Give the position of every malaria parasite.
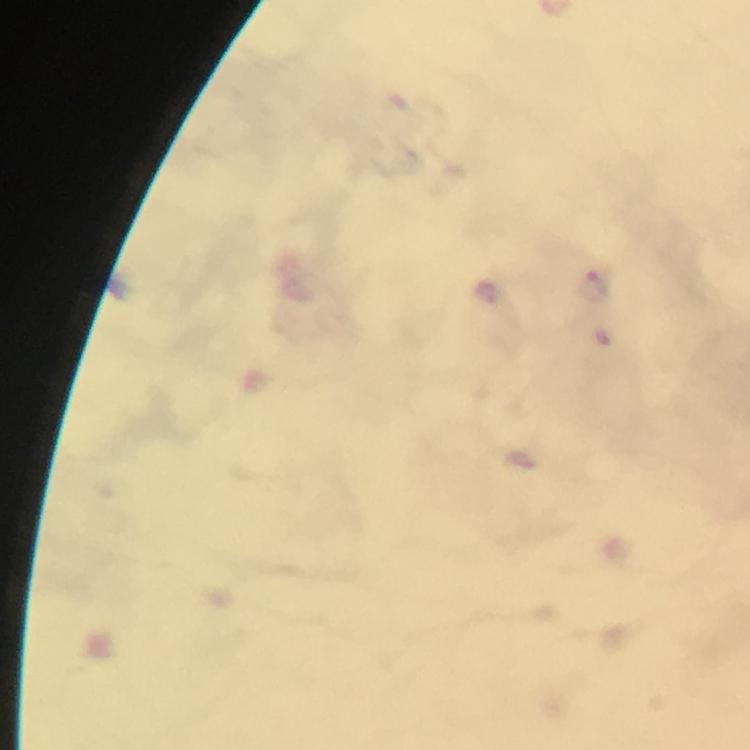

Approximate centers as {x, y} in pixels.
Malaria parasites: {593, 283}, {487, 294}.

100x magnification. From a malaria diagnostic workup. Smartphone photograph taken through a microscope. Cropped region of a single field of view. Giemsa stain. Immersion oil applied. Thick smear. Image is 750×750 pixels.